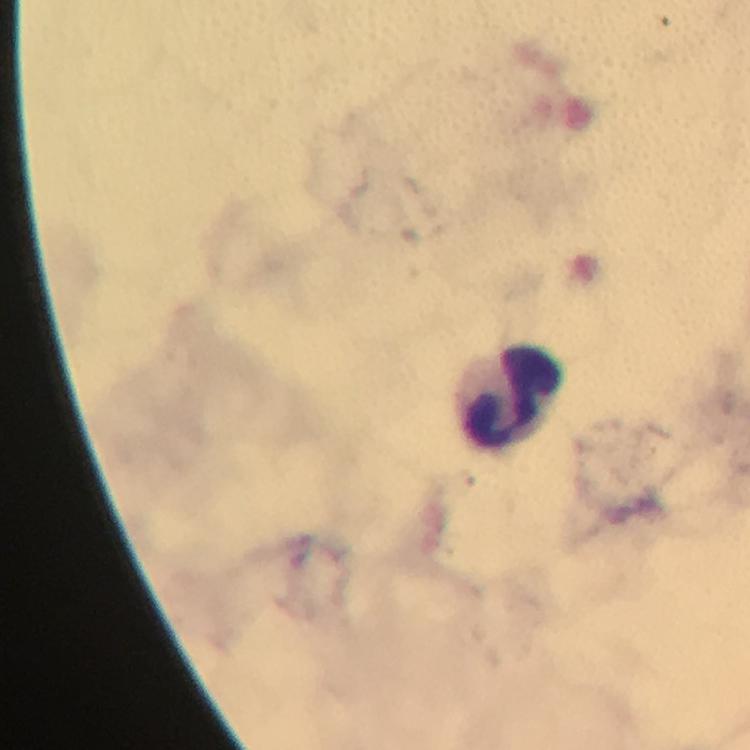

Approximate object centers, in pixels from the top-left corner. Leukocyte locations: (x=515, y=396). 100x magnification. Thick blood film. From a malaria diagnostic workup. Giemsa-stained preparation. Immersion oil applied. Image is 750×750 pixels. Malaria parasites: none seen. A crop from one field of view. Photographed with a smartphone mounted on the microscope.